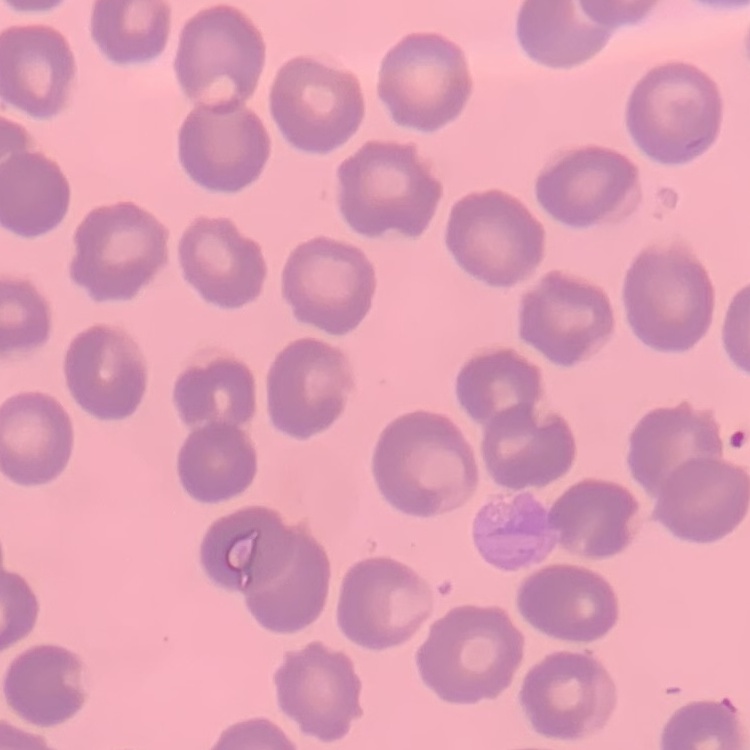
Summary:
  - Erythrocyte morphology: no rouleaux formation
  - Image type: square crop of a larger photomicrograph
  - Stain: Field's or Giemsa
  - Preparation: thin peripheral smear